Assess the morphology of the red blood cells.
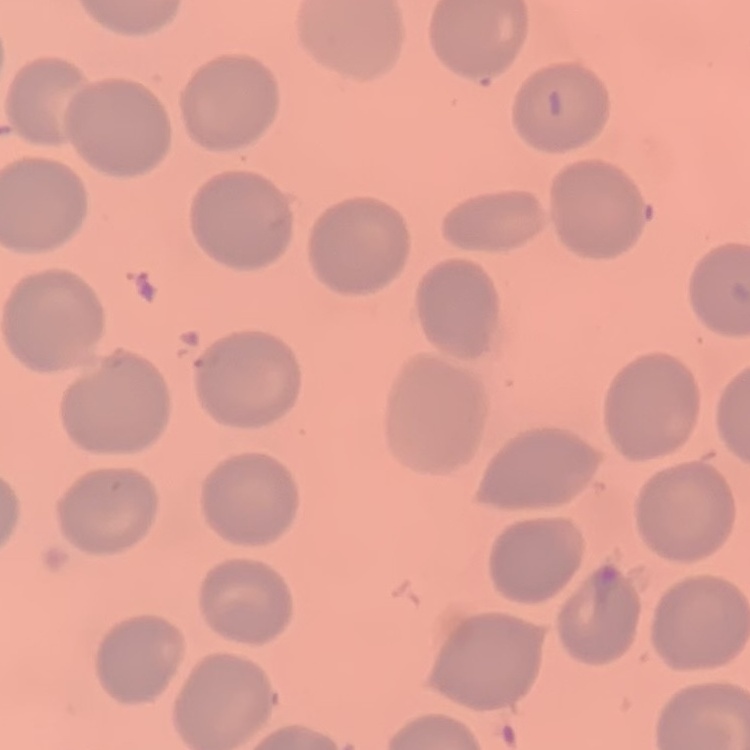

They show no rouleaux formation.

Summary:
  - Image type: one tile cut from a larger photomicrograph
  - Preparation: thin blood film
  - Stain: Field's or Giemsa